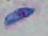
1000x magnification. Toxoplasma gondii is seen. Photomicrograph.